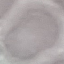
Summary:
  - Malaria status: uninfected
  - Preparation: thin blood smear
  - Image type: cell patch, automatically extracted from a larger field of view and resized to 64 × 64 pixels
  - Capture: smartphone through the microscope eyepiece
  - Stain: Giemsa